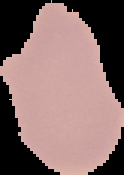
Summary:
  - Image size: 124×175 pixels
  - Result: negative for malaria parasites
  - Preparation: thin blood film
  - Image type: segmented cell region on a black background